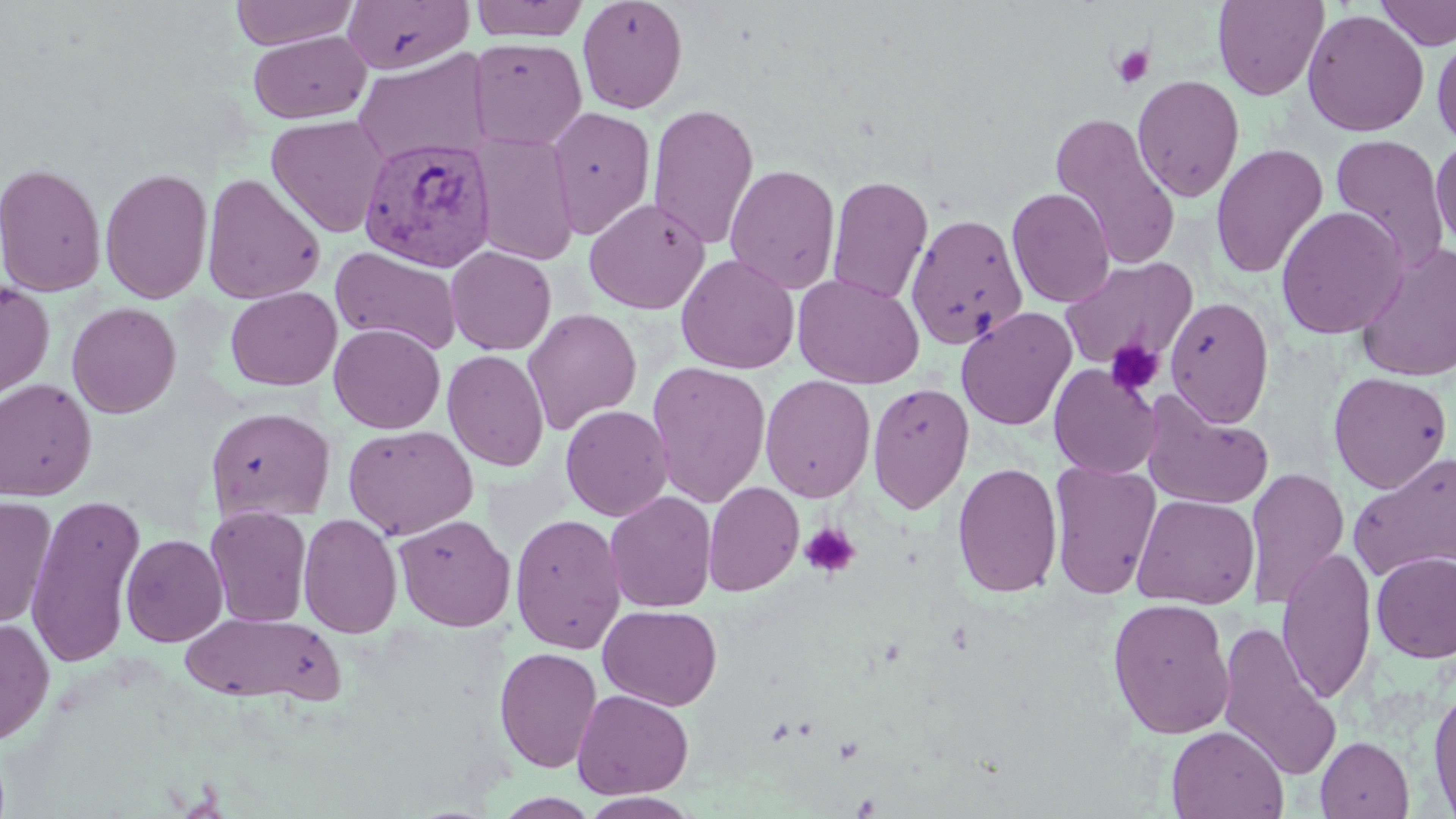

slide_level_diagnosis: Plasmodium vivax
image_size: 1456×819 pixels
modality: light microscopy
uninfected_red_blood_cell_locations: 'approximate bounding boxes as [x1, y1, x2, y2] in pixels: [231, 0, 358, 50], [342, 0, 474, 74], [469, 0, 589, 42], [577, 0, 688, 114], [1212, 0, 1328, 101], [1375, 0, 1456, 51], [1302, 8, 1429, 138], [249, 30, 370, 123], [1432, 31, 1456, 150], [468, 38, 587, 150], [352, 51, 490, 166], [1131, 74, 1245, 202], [647, 102, 759, 250], [546, 105, 656, 240], [1049, 112, 1181, 270], [266, 115, 390, 237], [471, 133, 579, 266], [1329, 133, 1450, 272], [1430, 137, 1456, 254], [1210, 143, 1329, 280], [0, 162, 107, 298], [725, 162, 840, 294], [100, 168, 213, 304], [202, 173, 327, 305], [826, 175, 933, 305], [1006, 187, 1115, 308], [584, 197, 710, 315], [1276, 206, 1408, 339], [905, 213, 1029, 350], [1356, 243, 1456, 383], [330, 245, 462, 357], [445, 246, 556, 355], [676, 253, 800, 374], [1059, 256, 1198, 371], [792, 273, 925, 389], [0, 280, 55, 403], [225, 286, 342, 391], [1165, 296, 1275, 427], [66, 301, 181, 418], [956, 306, 1077, 431], [523, 308, 642, 434], [329, 323, 446, 434], [442, 349, 549, 471], [647, 360, 771, 508], [1049, 364, 1161, 479], [1328, 371, 1453, 494], [759, 375, 876, 502], [0, 378, 97, 500], [867, 381, 974, 514], [1141, 393, 1274, 509], [560, 404, 673, 521], [205, 406, 336, 522], [343, 424, 478, 540], [1348, 450, 1456, 583], [1049, 460, 1161, 599], [952, 462, 1063, 598], [1244, 467, 1350, 608], [704, 481, 804, 597], [604, 490, 718, 613], [25, 492, 146, 669], [1131, 493, 1260, 608], [0, 496, 58, 628], [205, 506, 313, 628], [297, 513, 403, 638], [510, 513, 627, 655], [393, 514, 516, 631], [120, 533, 228, 647], [1277, 546, 1376, 704], [1371, 552, 1456, 663], [1107, 597, 1235, 739], [598, 604, 722, 710], [180, 611, 344, 706], [0, 618, 54, 746], [1215, 620, 1342, 782], [495, 646, 603, 774], [1428, 681, 1456, 818], [572, 689, 693, 799], [1166, 725, 1288, 819], [1315, 735, 1414, 818], [493, 793, 602, 818], [579, 793, 701, 819]'
field_of_view: one of a larger specimen
platelet_locations: 'approximate bounding boxes as [x1, y1, x2, y2] in pixels: [1110, 44, 1154, 90], [1104, 339, 1164, 396], [799, 522, 861, 578]'
preparation: thin blood film
magnification: 1000x
plasmodium_vivax_infected_red_blood_cell_locations: 'approximate bounding boxes as [x1, y1, x2, y2] in pixels: [358, 135, 496, 272]'
stain: May-Grünwald-Giemsa